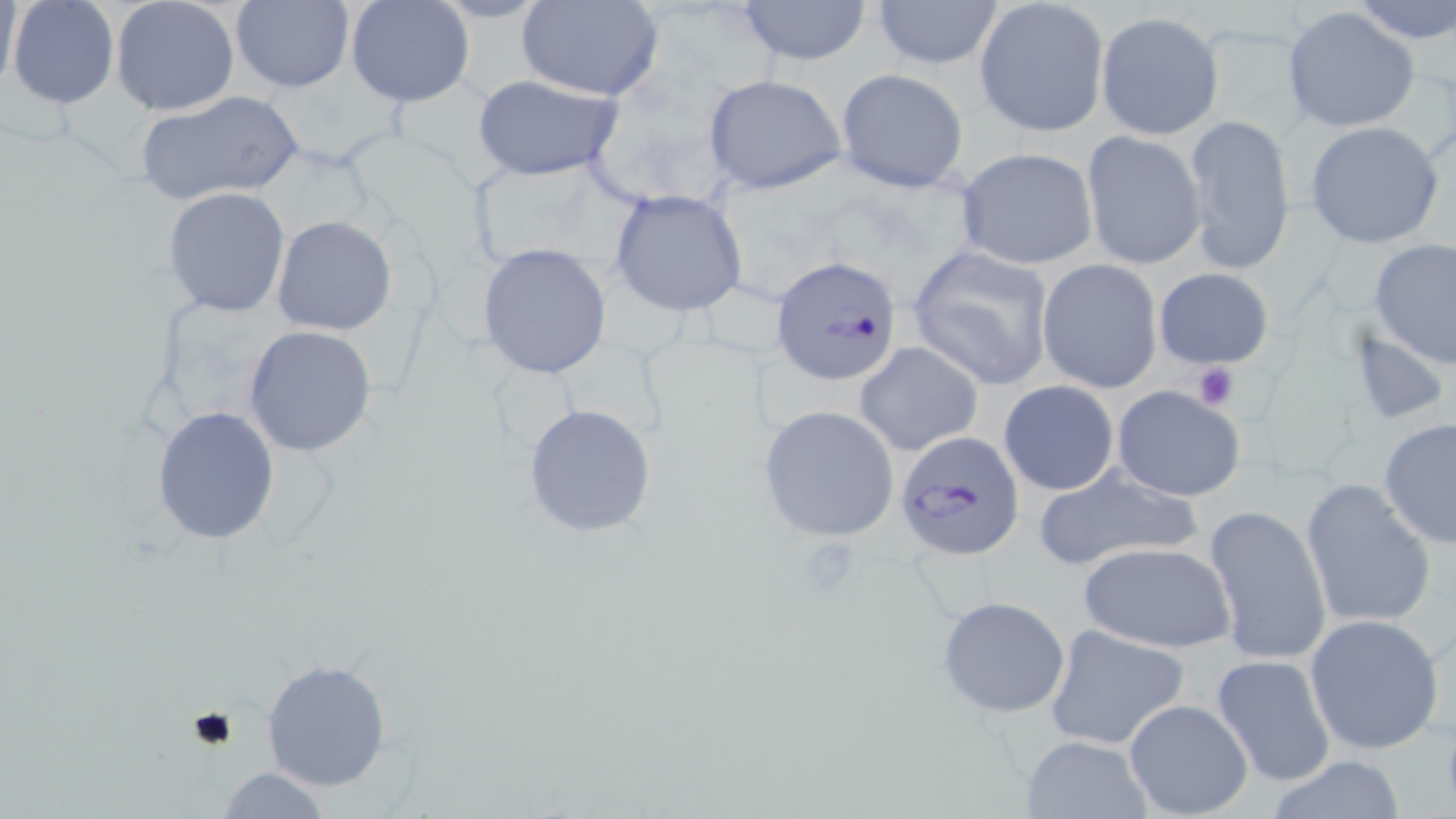
Summary:
  - Coordinate format: approximate bounding boxes as (x1,y1)-(x2,y2) corner pairs in pixels
  - Platelet locations: (1190,362)-(1240,411), (798,539)-(867,596), (186,705)-(241,754)
  - Uninfected red blood cell locations: (5,0)-(120,111), (110,0)-(240,117), (230,0)-(354,94), (347,0)-(474,107), (517,0)-(666,101), (735,0)-(873,66), (870,0)-(1003,72), (975,0)-(1108,136), (1344,0)-(1455,44), (1283,7)-(1419,132), (1095,11)-(1224,138), (834,67)-(969,192), (701,73)-(846,195), (472,74)-(626,182), (135,89)-(305,204), (1181,114)-(1298,273), (1305,121)-(1443,248), (1080,130)-(1206,270), (954,146)-(1099,270), (162,186)-(290,317), (607,188)-(751,317), (272,214)-(398,336), (1369,239)-(1456,371), (477,241)-(614,380), (907,244)-(1057,391), (1037,258)-(1163,393), (1153,268)-(1274,369), (244,326)-(378,456), (1346,326)-(1453,427), (854,341)-(983,457), (997,380)-(1120,496), (1111,385)-(1246,501), (521,402)-(659,539), (757,404)-(902,542), (152,406)-(281,546), (1379,418)-(1456,549), (1029,463)-(1208,575), (1301,477)-(1435,631), (1204,503)-(1331,668), (1078,542)-(1236,654), (936,596)-(1072,718), (1305,614)-(1445,755), (1044,623)-(1191,751), (1211,654)-(1337,787), (261,658)-(393,793), (1123,698)-(1254,818), (1016,735)-(1153,819), (1262,756)-(1412,818), (212,766)-(334,819)
  - Plasmodium falciparum-infected red blood cell locations: (771,253)-(903,386), (896,431)-(1023,558)
  - Slide-level diagnosis: Plasmodium falciparum
  - Field of view: single
  - Image size: 1456×819 pixels
  - Modality: light microscopy
  - Magnification: 1000x
  - Stain: May-Grünwald-Giemsa
  - Preparation: thin blood smear